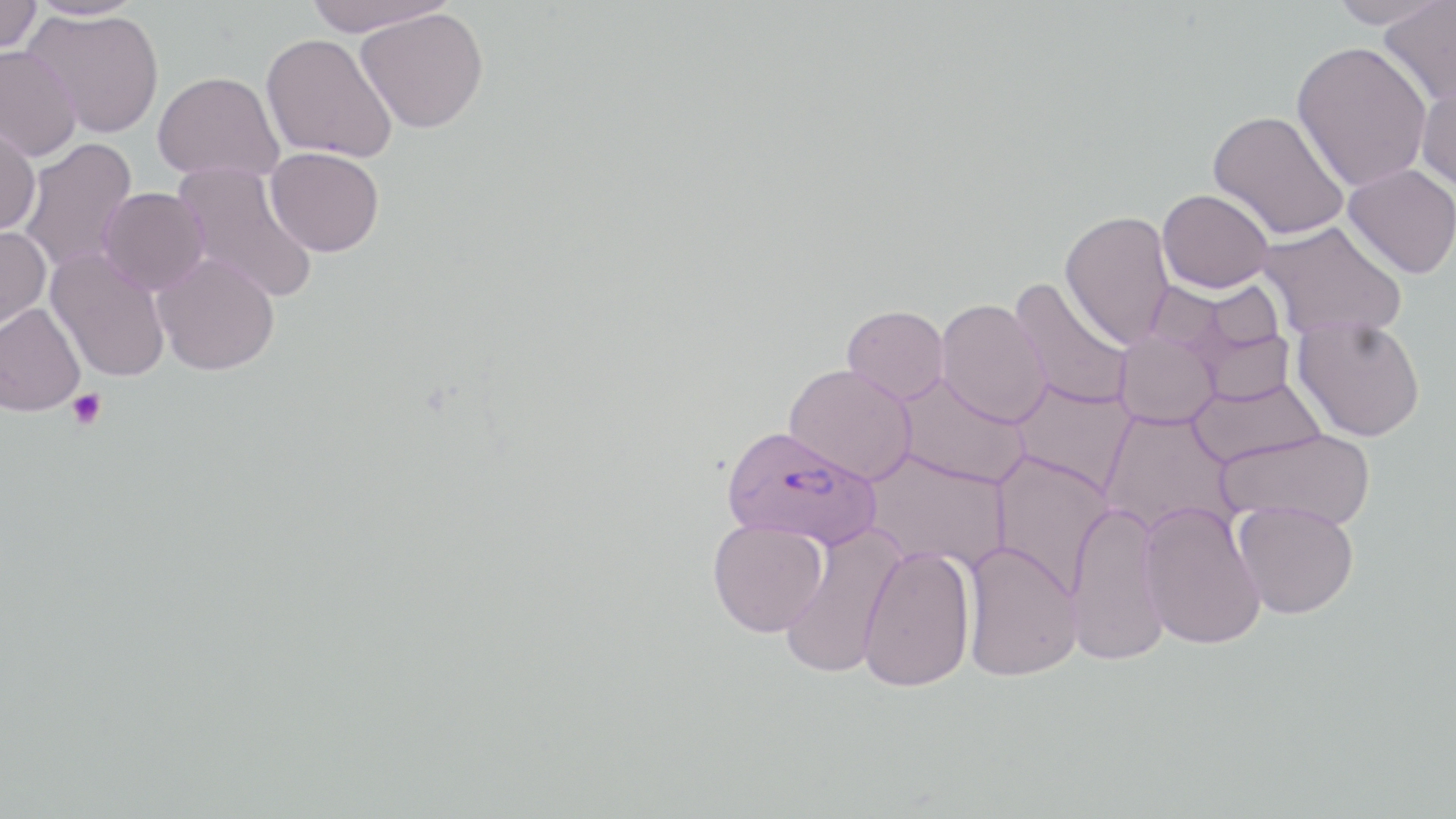
Summary:
  - Coordinate format: approximate bounding boxes as (x1,y1)-(x2,y2) corner pairs in pixels
  - Platelet locations: (68,388)-(107,430)
  - Plasmodium falciparum-infected red blood cell locations: (720,424)-(881,550)
  - Uninfected red blood cell locations: (0,0)-(43,54), (27,0)-(146,20), (302,0)-(455,36), (1325,0)-(1450,29), (1378,2)-(1456,108), (23,8)-(164,139), (356,8)-(489,133), (261,33)-(397,162), (1291,41)-(1433,191), (0,45)-(82,162), (153,71)-(284,182), (1416,78)-(1456,194), (1208,110)-(1349,241), (0,119)-(41,236), (18,138)-(139,274), (265,147)-(385,256), (171,162)-(318,304), (1343,164)-(1456,278), (99,187)-(209,295), (1157,189)-(1274,293), (1060,210)-(1174,348), (1257,220)-(1407,339), (0,225)-(52,332), (47,247)-(171,383), (152,252)-(280,375), (1008,277)-(1133,411), (1171,286)-(1297,402), (936,298)-(1051,427), (0,303)-(85,416), (842,305)-(949,404), (1292,315)-(1426,441), (1114,330)-(1221,429), (783,363)-(917,484), (893,372)-(1031,489), (1188,377)-(1326,468), (1011,378)-(1136,495), (1100,409)-(1238,537), (1215,428)-(1376,530), (862,449)-(1011,572), (989,451)-(1116,597), (1233,500)-(1359,619), (1066,501)-(1170,666), (1139,502)-(1266,650), (708,519)-(828,637), (779,524)-(904,679), (963,541)-(1083,681), (858,545)-(976,692)
  - Slide-level diagnosis: Plasmodium falciparum
  - Image size: 1456×819 pixels
  - Magnification: 1000x
  - Modality: optical microscopy
  - Stain: May-Grünwald-Giemsa
  - Field of view: one of a larger specimen
  - Preparation: thin blood film